Assess this cell for malaria.
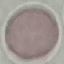
It is uninfected.

Thin smear of blood. Giemsa stain. Cell patch, automatically extracted from a larger field of view and resized to 64 × 64 pixels. Acquired by smartphone through the microscope eyepiece.